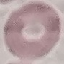
Malaria status: uninfected. Giemsa-stained preparation. Automatically extracted cell patch, resized to 64 × 64 pixels. Thin blood smear. Photographed with a smartphone camera at the microscope eyepiece.